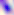
Summary:
  - Modality: photomicrograph
  - Identification: Toxoplasma gondii
  - Magnification: 400x